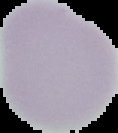
Summary:
  - Image type: segmented cell region on a black background
  - Image size: 118×133 pixels
  - Preparation: thin blood smear
  - Malaria status: uninfected